Report the malaria status of this cell.
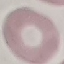
It is uninfected.

Acquired by smartphone through the microscope eyepiece. Automatically extracted cell patch, resized to 64 × 64 pixels. Thin blood smear. Giemsa-stained preparation.